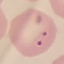

{
  "result": "malaria parasites identified",
  "preparation": "thin smear",
  "stain": "Giemsa",
  "image_type": "automatically extracted cell patch, resized to 64 × 64 pixels",
  "capture": "smartphone through the microscope eyepiece"
}